Assess this cell for malaria.
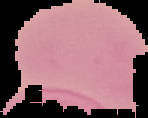

It is uninfected.

From a thin blood smear. Image is 148×118 pixels. The area outside the segmented cell region is set to black.